Outline each blood parasite and name the species.
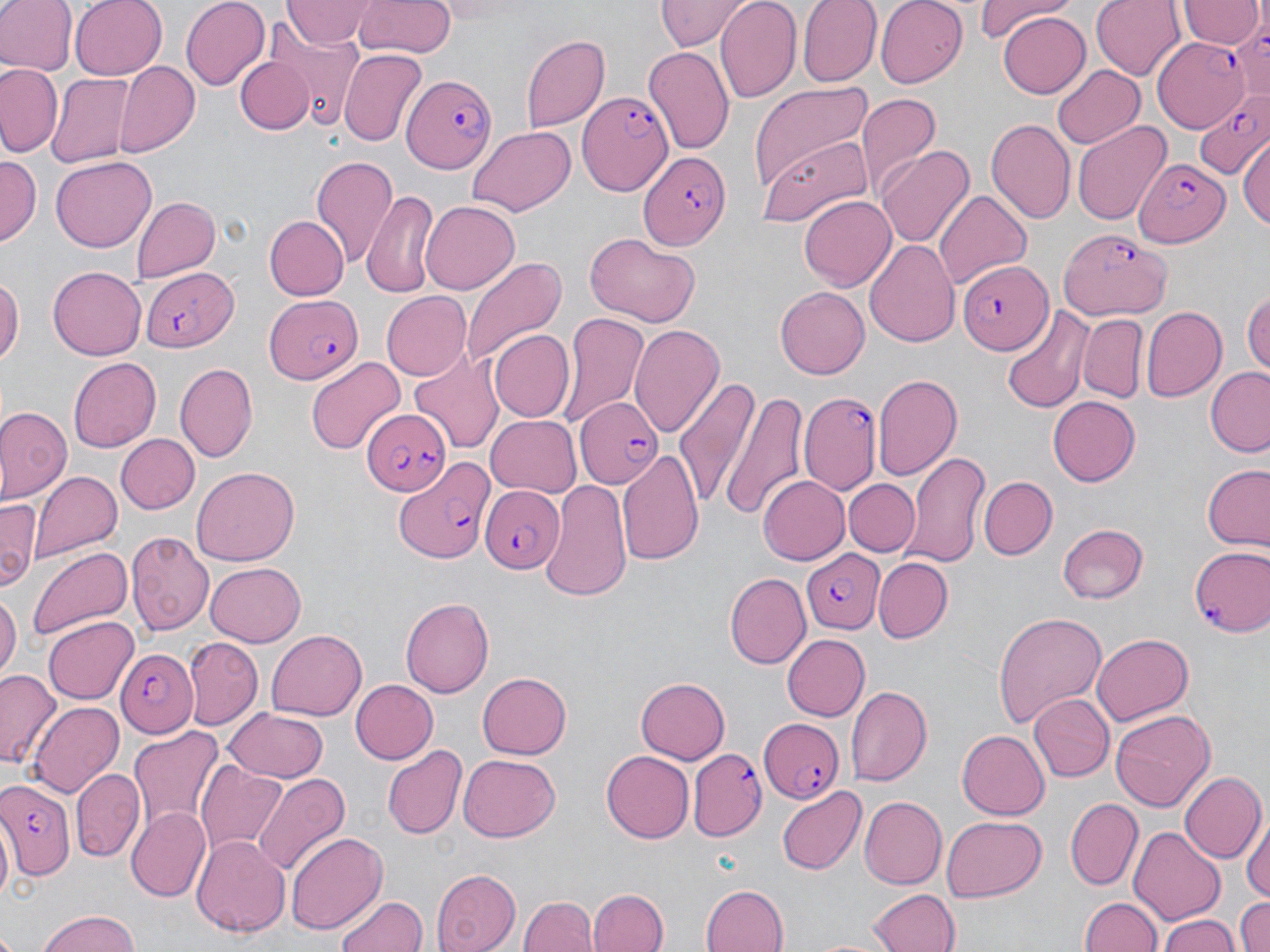

Approximate bounding boxes as named x1/y1/x2/y2 corners in pixels.
Plasmodium falciparum-infected red blood cells: (x1=1154, y1=37, x2=1249, y2=129), (x1=403, y1=75, x2=497, y2=174), (x1=1191, y1=90, x2=1270, y2=181), (x1=577, y1=93, x2=675, y2=199), (x1=1128, y1=151, x2=1232, y2=247), (x1=639, y1=152, x2=730, y2=250), (x1=1057, y1=228, x2=1171, y2=320), (x1=960, y1=259, x2=1052, y2=356), (x1=142, y1=266, x2=238, y2=350), (x1=265, y1=293, x2=364, y2=386), (x1=798, y1=391, x2=881, y2=493), (x1=575, y1=396, x2=664, y2=486), (x1=361, y1=409, x2=449, y2=494), (x1=393, y1=459, x2=491, y2=565), (x1=479, y1=482, x2=564, y2=572), (x1=1187, y1=545, x2=1270, y2=640), (x1=801, y1=546, x2=887, y2=634), (x1=115, y1=648, x2=198, y2=738), (x1=758, y1=715, x2=846, y2=802), (x1=687, y1=749, x2=765, y2=840), (x1=0, y1=779, x2=73, y2=881).
No Plasmodium ovale, Plasmodium malariae, Plasmodium vivax, Babesia divergens, or Trypanosoma brucei observed.

Summary:
  - Uninfected red blood cell locations: (x1=0, y1=0, x2=75, y2=75), (x1=69, y1=0, x2=167, y2=79), (x1=181, y1=0, x2=269, y2=89), (x1=353, y1=0, x2=456, y2=58), (x1=656, y1=0, x2=751, y2=51), (x1=797, y1=0, x2=878, y2=87), (x1=875, y1=0, x2=969, y2=88), (x1=976, y1=0, x2=1074, y2=43), (x1=1090, y1=0, x2=1185, y2=78), (x1=716, y1=1, x2=802, y2=104), (x1=1181, y1=1, x2=1260, y2=48), (x1=282, y1=2, x2=374, y2=48), (x1=996, y1=11, x2=1091, y2=97), (x1=254, y1=29, x2=362, y2=133), (x1=519, y1=33, x2=611, y2=134), (x1=643, y1=45, x2=735, y2=154), (x1=337, y1=49, x2=426, y2=147), (x1=236, y1=54, x2=315, y2=135), (x1=116, y1=61, x2=200, y2=154), (x1=0, y1=63, x2=64, y2=157), (x1=1052, y1=63, x2=1146, y2=148), (x1=48, y1=73, x2=134, y2=170), (x1=749, y1=82, x2=877, y2=197), (x1=854, y1=92, x2=941, y2=194), (x1=986, y1=117, x2=1076, y2=223), (x1=1070, y1=119, x2=1171, y2=228), (x1=465, y1=127, x2=574, y2=216), (x1=757, y1=133, x2=873, y2=226), (x1=1240, y1=135, x2=1270, y2=233), (x1=875, y1=147, x2=974, y2=249), (x1=310, y1=153, x2=399, y2=271), (x1=51, y1=154, x2=155, y2=250), (x1=1, y1=156, x2=39, y2=246), (x1=362, y1=189, x2=441, y2=297), (x1=934, y1=190, x2=1032, y2=288), (x1=800, y1=194, x2=896, y2=290), (x1=132, y1=197, x2=220, y2=283), (x1=420, y1=200, x2=519, y2=294), (x1=263, y1=216, x2=349, y2=299), (x1=584, y1=233, x2=699, y2=328), (x1=865, y1=237, x2=961, y2=349), (x1=460, y1=257, x2=564, y2=371), (x1=47, y1=266, x2=145, y2=360), (x1=0, y1=273, x2=23, y2=366), (x1=1244, y1=285, x2=1270, y2=378), (x1=775, y1=286, x2=869, y2=379), (x1=381, y1=292, x2=472, y2=378), (x1=998, y1=305, x2=1094, y2=414), (x1=1143, y1=306, x2=1227, y2=401), (x1=556, y1=313, x2=650, y2=430), (x1=1078, y1=314, x2=1147, y2=403), (x1=631, y1=324, x2=725, y2=437), (x1=488, y1=330, x2=574, y2=423), (x1=409, y1=352, x2=505, y2=456), (x1=68, y1=355, x2=161, y2=452), (x1=306, y1=356, x2=406, y2=455), (x1=173, y1=362, x2=257, y2=462), (x1=1205, y1=369, x2=1270, y2=459), (x1=674, y1=372, x2=757, y2=511), (x1=872, y1=374, x2=964, y2=483), (x1=718, y1=390, x2=808, y2=521), (x1=1048, y1=396, x2=1142, y2=487), (x1=0, y1=407, x2=70, y2=501), (x1=485, y1=416, x2=580, y2=497), (x1=115, y1=434, x2=200, y2=515), (x1=617, y1=449, x2=706, y2=568), (x1=902, y1=451, x2=990, y2=568), (x1=1202, y1=462, x2=1270, y2=551), (x1=192, y1=466, x2=299, y2=565), (x1=30, y1=471, x2=120, y2=564), (x1=756, y1=475, x2=849, y2=566), (x1=977, y1=476, x2=1058, y2=559), (x1=843, y1=478, x2=920, y2=556), (x1=542, y1=480, x2=630, y2=599), (x1=0, y1=497, x2=41, y2=592), (x1=1056, y1=522, x2=1148, y2=605), (x1=126, y1=531, x2=212, y2=633), (x1=25, y1=543, x2=133, y2=646), (x1=872, y1=556, x2=953, y2=642), (x1=203, y1=564, x2=308, y2=646), (x1=724, y1=573, x2=810, y2=668), (x1=0, y1=591, x2=19, y2=679), (x1=401, y1=597, x2=494, y2=696), (x1=994, y1=612, x2=1105, y2=727), (x1=41, y1=615, x2=139, y2=704), (x1=265, y1=629, x2=370, y2=722), (x1=1091, y1=633, x2=1195, y2=726), (x1=782, y1=634, x2=872, y2=721), (x1=184, y1=636, x2=262, y2=727), (x1=0, y1=668, x2=62, y2=771), (x1=477, y1=672, x2=572, y2=758), (x1=637, y1=675, x2=731, y2=764), (x1=347, y1=678, x2=438, y2=765), (x1=846, y1=684, x2=933, y2=786), (x1=1028, y1=692, x2=1114, y2=783), (x1=27, y1=700, x2=125, y2=799), (x1=224, y1=707, x2=329, y2=783), (x1=1110, y1=709, x2=1215, y2=811), (x1=129, y1=726, x2=223, y2=833), (x1=958, y1=730, x2=1050, y2=820), (x1=382, y1=745, x2=466, y2=841), (x1=601, y1=751, x2=694, y2=843), (x1=457, y1=754, x2=562, y2=842), (x1=197, y1=762, x2=290, y2=852), (x1=72, y1=768, x2=144, y2=860), (x1=252, y1=771, x2=351, y2=876), (x1=1180, y1=771, x2=1266, y2=865), (x1=776, y1=784, x2=869, y2=873), (x1=859, y1=796, x2=946, y2=887), (x1=1064, y1=798, x2=1142, y2=890), (x1=125, y1=807, x2=210, y2=903), (x1=943, y1=816, x2=1046, y2=902), (x1=1245, y1=817, x2=1269, y2=907), (x1=1130, y1=826, x2=1223, y2=927), (x1=288, y1=831, x2=386, y2=937), (x1=193, y1=833, x2=289, y2=937), (x1=432, y1=869, x2=519, y2=952), (x1=700, y1=884, x2=789, y2=952), (x1=589, y1=889, x2=667, y2=952), (x1=867, y1=889, x2=960, y2=952), (x1=336, y1=892, x2=428, y2=952), (x1=520, y1=895, x2=596, y2=952), (x1=1078, y1=896, x2=1165, y2=952), (x1=1234, y1=897, x2=1270, y2=952), (x1=35, y1=910, x2=144, y2=951), (x1=1159, y1=912, x2=1241, y2=952)
  - Slide-level diagnosis: Plasmodium falciparum
  - Field of view: single
  - Image size: 1270×952 pixels
  - Magnification: 1000x
  - Modality: optical microscopy
  - Preparation: thin blood smear
  - Stain: May-Grünwald-Giemsa